Give the extent of all Plasmodium ovale-infected red blood cells.
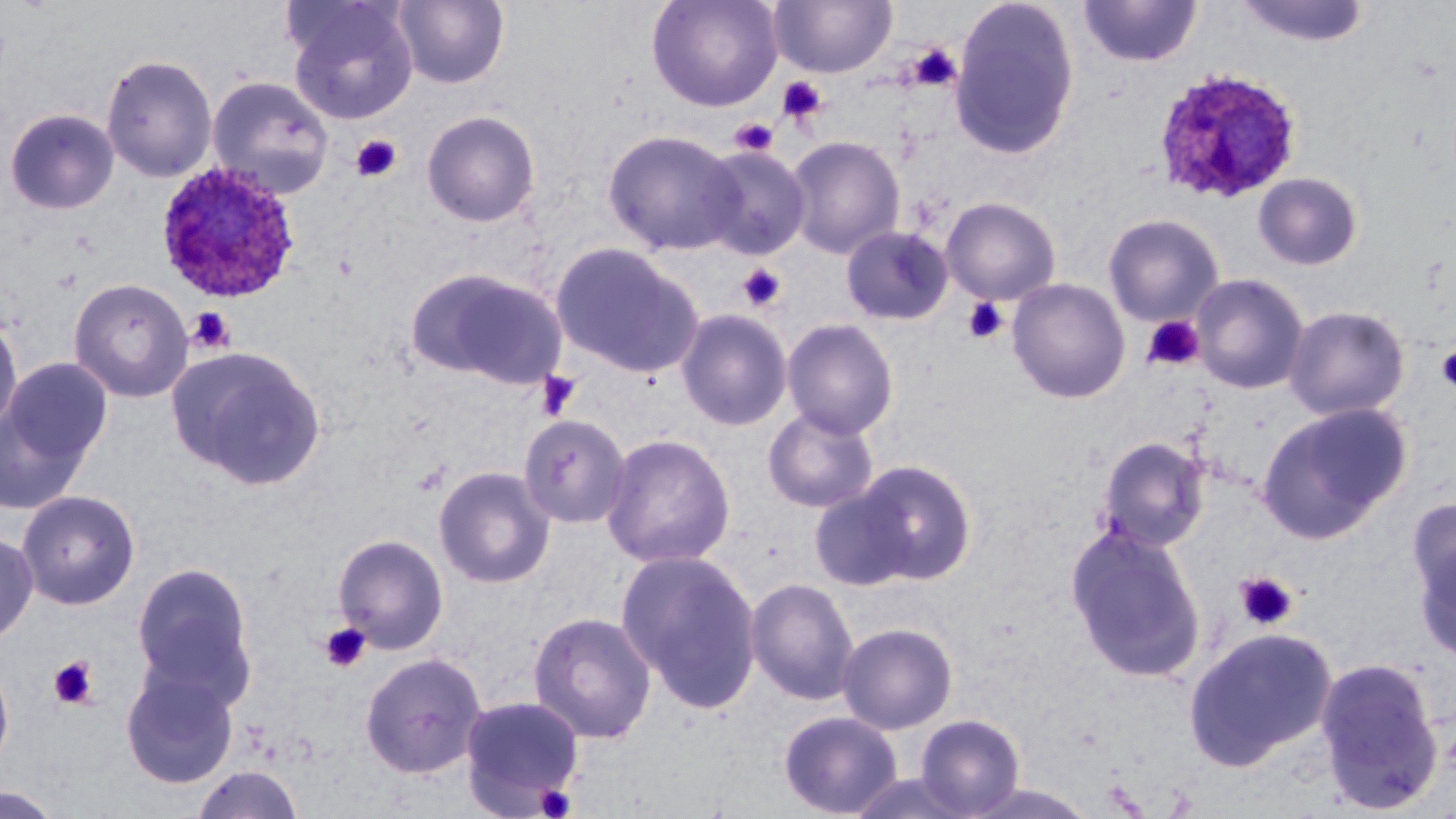

Approximate bounding boxes as named x1/y1/x2/y2 corners in pixels.
Plasmodium ovale-infected red blood cells: (x1=1152, y1=67, x2=1303, y2=205), (x1=154, y1=161, x2=303, y2=304).

Uninfected red blood cell locations: (x1=284, y1=0, x2=419, y2=124), (x1=392, y1=0, x2=510, y2=89), (x1=646, y1=0, x2=783, y2=113), (x1=768, y1=0, x2=897, y2=79), (x1=1078, y1=0, x2=1202, y2=68), (x1=1235, y1=0, x2=1371, y2=48), (x1=949, y1=1, x2=1080, y2=160), (x1=101, y1=54, x2=218, y2=182), (x1=206, y1=74, x2=335, y2=199), (x1=4, y1=108, x2=120, y2=215), (x1=421, y1=109, x2=541, y2=227), (x1=602, y1=128, x2=743, y2=256), (x1=785, y1=134, x2=905, y2=258), (x1=697, y1=145, x2=811, y2=259), (x1=1252, y1=172, x2=1364, y2=271), (x1=940, y1=197, x2=1061, y2=305), (x1=1103, y1=213, x2=1224, y2=327), (x1=840, y1=225, x2=953, y2=326), (x1=551, y1=242, x2=704, y2=379), (x1=405, y1=267, x2=564, y2=387), (x1=1189, y1=273, x2=1309, y2=395), (x1=68, y1=277, x2=193, y2=403), (x1=1007, y1=278, x2=1130, y2=404), (x1=1284, y1=305, x2=1410, y2=421), (x1=675, y1=308, x2=794, y2=431), (x1=0, y1=312, x2=23, y2=438), (x1=781, y1=318, x2=899, y2=440), (x1=165, y1=344, x2=327, y2=490), (x1=2, y1=357, x2=113, y2=473), (x1=0, y1=398, x2=93, y2=516), (x1=1257, y1=402, x2=1412, y2=543), (x1=762, y1=407, x2=879, y2=513), (x1=518, y1=414, x2=630, y2=530), (x1=600, y1=432, x2=736, y2=568), (x1=1097, y1=435, x2=1210, y2=552), (x1=855, y1=459, x2=977, y2=584), (x1=433, y1=465, x2=556, y2=589), (x1=808, y1=486, x2=915, y2=591), (x1=16, y1=489, x2=141, y2=610), (x1=1408, y1=497, x2=1456, y2=654), (x1=1064, y1=524, x2=1206, y2=682), (x1=0, y1=530, x2=38, y2=645), (x1=332, y1=533, x2=449, y2=654), (x1=615, y1=548, x2=763, y2=714), (x1=130, y1=560, x2=258, y2=709), (x1=745, y1=577, x2=860, y2=705), (x1=528, y1=611, x2=657, y2=744), (x1=837, y1=622, x2=958, y2=733), (x1=1183, y1=627, x2=1337, y2=770), (x1=359, y1=652, x2=487, y2=779), (x1=1313, y1=656, x2=1445, y2=815), (x1=0, y1=657, x2=14, y2=778), (x1=120, y1=666, x2=240, y2=789), (x1=459, y1=695, x2=584, y2=815), (x1=778, y1=710, x2=903, y2=818), (x1=914, y1=713, x2=1025, y2=816), (x1=190, y1=764, x2=305, y2=819), (x1=845, y1=772, x2=979, y2=818), (x1=1, y1=785, x2=66, y2=819). Platelet locations: (x1=908, y1=43, x2=962, y2=92), (x1=777, y1=76, x2=828, y2=126), (x1=729, y1=117, x2=779, y2=157), (x1=350, y1=134, x2=402, y2=183), (x1=738, y1=263, x2=786, y2=312), (x1=963, y1=296, x2=1009, y2=345), (x1=187, y1=307, x2=236, y2=355), (x1=1141, y1=315, x2=1205, y2=372), (x1=1435, y1=345, x2=1456, y2=393), (x1=535, y1=370, x2=582, y2=421), (x1=412, y1=460, x2=450, y2=497), (x1=1234, y1=572, x2=1298, y2=630), (x1=319, y1=623, x2=371, y2=673), (x1=48, y1=656, x2=99, y2=710), (x1=534, y1=784, x2=577, y2=818). Slide-level diagnosis: Plasmodium ovale. 1000x magnification. Light microscopy. Thin blood film. One field of a larger specimen. Image is 1456×819 pixels. May-Grünwald-Giemsa-stained preparation.